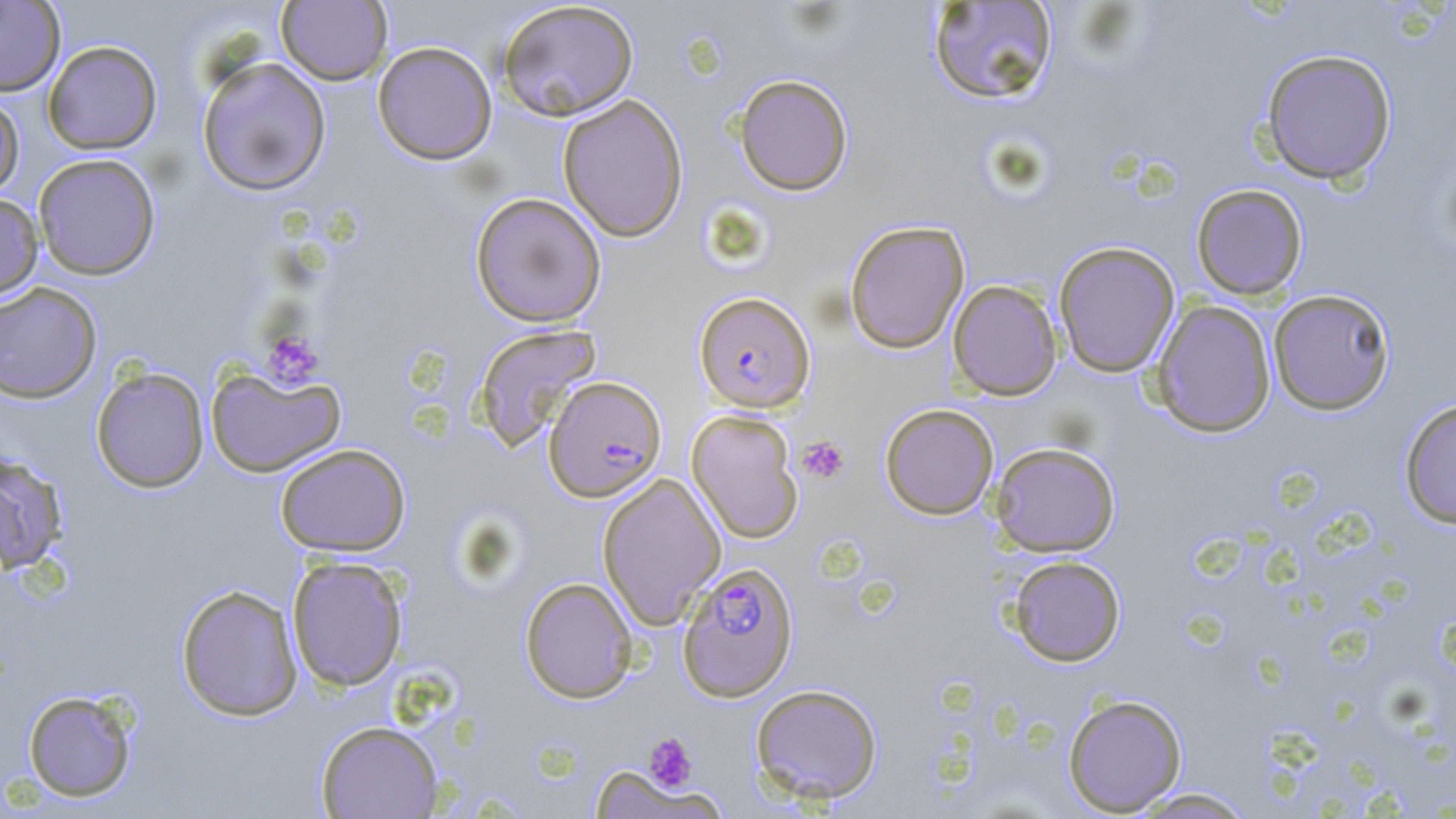

slide-level diagnosis = Plasmodium falciparum
uninfected red blood cell locations = approximate bounding boxes as named x1/y1/x2/y2 corners in pixels: (x1=0, y1=0, x2=66, y2=96), (x1=497, y1=0, x2=639, y2=121), (x1=276, y1=1, x2=393, y2=86), (x1=926, y1=2, x2=1060, y2=106), (x1=43, y1=40, x2=163, y2=154), (x1=372, y1=41, x2=497, y2=165), (x1=1260, y1=48, x2=1397, y2=185), (x1=196, y1=56, x2=332, y2=196), (x1=734, y1=73, x2=854, y2=196), (x1=0, y1=89, x2=25, y2=201), (x1=557, y1=93, x2=689, y2=242), (x1=33, y1=153, x2=161, y2=280), (x1=1191, y1=184, x2=1309, y2=300), (x1=470, y1=192, x2=607, y2=327), (x1=0, y1=193, x2=44, y2=301), (x1=844, y1=220, x2=969, y2=354), (x1=1053, y1=241, x2=1180, y2=377), (x1=947, y1=279, x2=1063, y2=401), (x1=0, y1=282, x2=102, y2=404), (x1=1267, y1=289, x2=1396, y2=415), (x1=1152, y1=300, x2=1276, y2=438), (x1=472, y1=323, x2=603, y2=452), (x1=206, y1=365, x2=345, y2=478), (x1=91, y1=366, x2=209, y2=493), (x1=1399, y1=397, x2=1456, y2=529), (x1=880, y1=404, x2=999, y2=520), (x1=686, y1=410, x2=804, y2=543), (x1=990, y1=442, x2=1121, y2=557), (x1=275, y1=443, x2=411, y2=556), (x1=0, y1=451, x2=69, y2=574), (x1=598, y1=473, x2=726, y2=629), (x1=1007, y1=555, x2=1126, y2=666), (x1=286, y1=556, x2=408, y2=691), (x1=519, y1=577, x2=638, y2=703), (x1=176, y1=583, x2=304, y2=721), (x1=750, y1=683, x2=883, y2=804), (x1=22, y1=688, x2=139, y2=803), (x1=1062, y1=694, x2=1188, y2=815), (x1=316, y1=720, x2=443, y2=818), (x1=589, y1=765, x2=718, y2=818), (x1=1125, y1=787, x2=1258, y2=818)
field of view = one of a larger specimen
platelet locations = approximate bounding boxes as named x1/y1/x2/y2 corners in pixels: (x1=261, y1=330, x2=325, y2=389), (x1=796, y1=435, x2=850, y2=485), (x1=643, y1=731, x2=698, y2=793)
preparation = thin blood smear
magnification = 1000x
modality = optical microscopy
image size = 1456×819 pixels
stain = May-Grünwald-Giemsa
Plasmodium falciparum-infected red blood cell locations = approximate bounding boxes as named x1/y1/x2/y2 corners in pixels: (x1=694, y1=292, x2=815, y2=412), (x1=543, y1=375, x2=667, y2=502), (x1=678, y1=560, x2=798, y2=701)